Identify the cell.
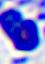
A leukocyte.

Summary:
  - Modality: micrograph
  - Magnification: 400x